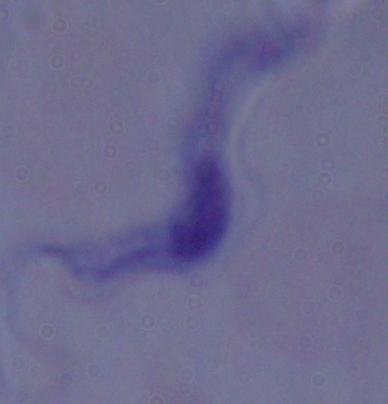
magnification = 1000x
identification = trypanosome
modality = photomicrograph